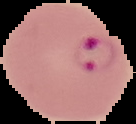

Summary:
  - Image size: 136×124 pixels
  - Image type: segmented cell region with the area outside set to black
  - Malaria status: parasitized
  - Preparation: thin blood smear